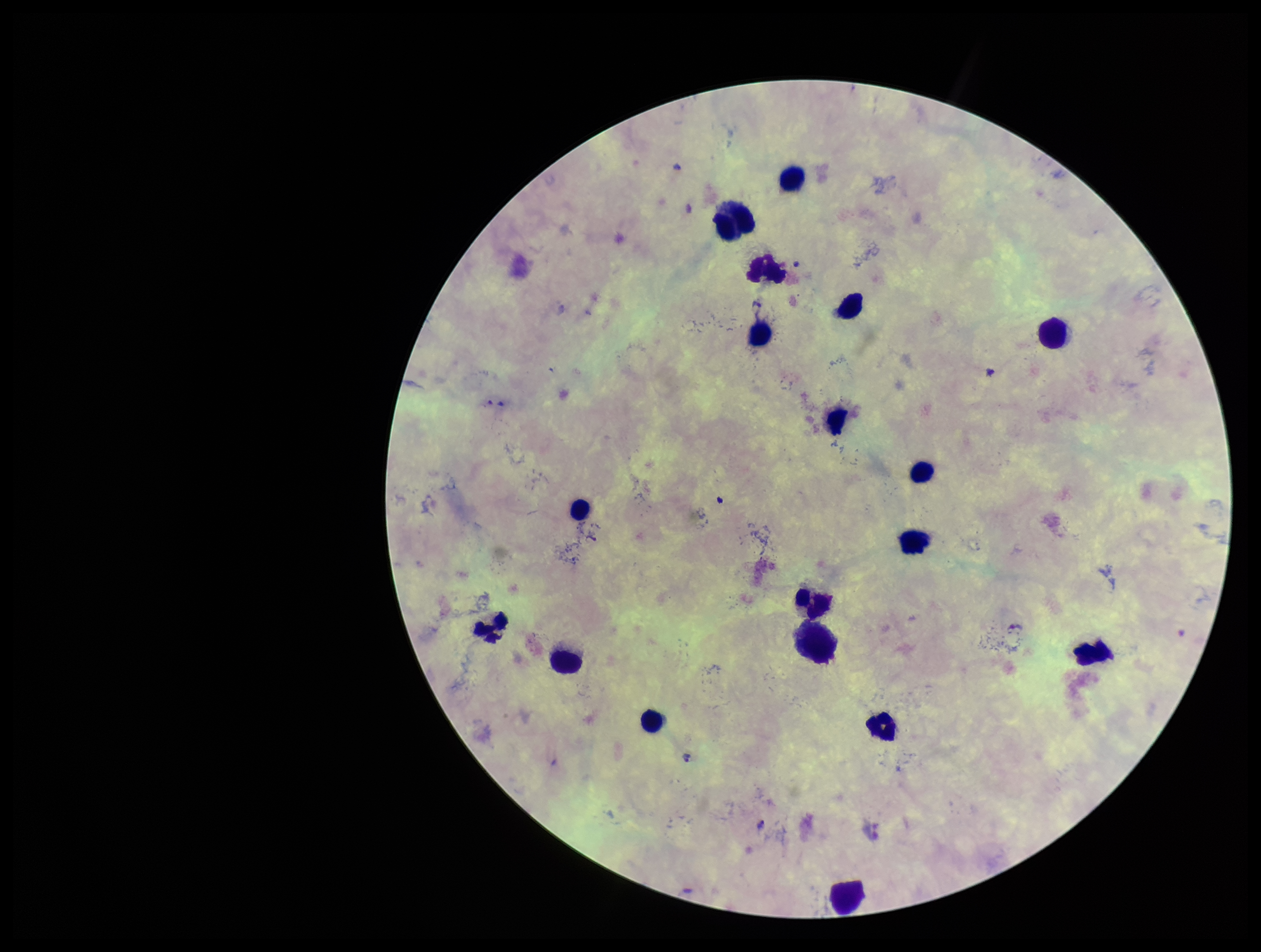 Species reported for this patient: Plasmodium falciparum. Image is 1261×952 pixels. Giemsa stain. Preparation: thick. Patient malaria status: infected. Leukocyte count: 18. Photographed through the microscope eyepiece with a smartphone camera. Single field of view. Parasite count: 2. Plasmodium parasites: detected.